Locate every Plasmodium ovale-infected red blood cell.
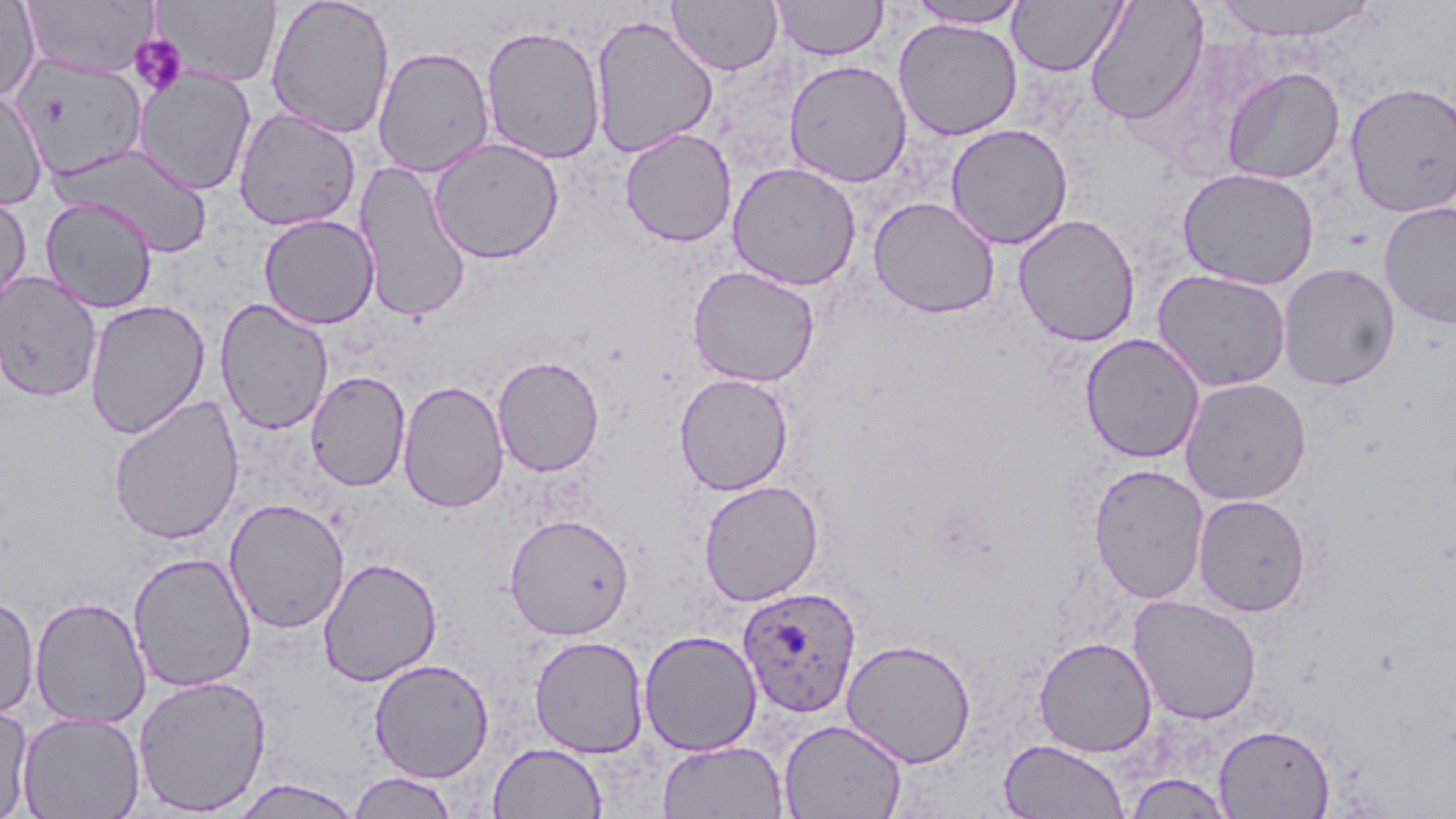
Approximate bounding boxes as named x1/y1/x2/y2 corners in pixels.
Plasmodium ovale-infected red blood cells: (x1=737, y1=587, x2=861, y2=718).

Summary:
  - Uninfected red blood cell locations: (x1=20, y1=0, x2=159, y2=79), (x1=153, y1=0, x2=284, y2=87), (x1=265, y1=0, x2=396, y2=138), (x1=772, y1=0, x2=887, y2=60), (x1=907, y1=0, x2=1030, y2=28), (x1=1007, y1=0, x2=1128, y2=76), (x1=1085, y1=0, x2=1209, y2=126), (x1=1211, y1=0, x2=1380, y2=41), (x1=0, y1=1, x2=41, y2=103), (x1=668, y1=1, x2=783, y2=75), (x1=589, y1=13, x2=720, y2=158), (x1=894, y1=18, x2=1023, y2=141), (x1=480, y1=24, x2=607, y2=165), (x1=372, y1=46, x2=495, y2=177), (x1=15, y1=56, x2=149, y2=173), (x1=784, y1=59, x2=913, y2=187), (x1=1222, y1=66, x2=1345, y2=184), (x1=133, y1=67, x2=257, y2=196), (x1=1345, y1=81, x2=1456, y2=217), (x1=0, y1=87, x2=49, y2=210), (x1=233, y1=107, x2=362, y2=231), (x1=945, y1=123, x2=1073, y2=250), (x1=619, y1=127, x2=737, y2=247), (x1=428, y1=137, x2=565, y2=264), (x1=54, y1=144, x2=214, y2=256), (x1=354, y1=159, x2=472, y2=324), (x1=727, y1=161, x2=862, y2=290), (x1=1178, y1=167, x2=1320, y2=290), (x1=0, y1=191, x2=32, y2=311), (x1=38, y1=196, x2=157, y2=313), (x1=868, y1=196, x2=1001, y2=319), (x1=1379, y1=202, x2=1456, y2=329), (x1=1013, y1=213, x2=1140, y2=347), (x1=258, y1=214, x2=380, y2=330), (x1=1277, y1=263, x2=1401, y2=390), (x1=687, y1=265, x2=821, y2=387), (x1=1152, y1=269, x2=1293, y2=392), (x1=0, y1=270, x2=102, y2=402), (x1=214, y1=298, x2=334, y2=435), (x1=84, y1=299, x2=211, y2=439), (x1=1079, y1=333, x2=1206, y2=463), (x1=492, y1=355, x2=605, y2=477), (x1=305, y1=370, x2=411, y2=491), (x1=674, y1=372, x2=794, y2=495), (x1=1179, y1=377, x2=1312, y2=506), (x1=398, y1=380, x2=510, y2=513), (x1=107, y1=393, x2=245, y2=545), (x1=1088, y1=463, x2=1210, y2=604), (x1=698, y1=480, x2=825, y2=606), (x1=1193, y1=494, x2=1312, y2=616), (x1=224, y1=498, x2=350, y2=634), (x1=504, y1=513, x2=635, y2=640), (x1=127, y1=552, x2=256, y2=693), (x1=318, y1=556, x2=443, y2=687), (x1=0, y1=593, x2=40, y2=718), (x1=1128, y1=594, x2=1263, y2=725), (x1=29, y1=596, x2=151, y2=729), (x1=638, y1=629, x2=762, y2=756), (x1=529, y1=635, x2=649, y2=758), (x1=1033, y1=636, x2=1158, y2=757), (x1=840, y1=638, x2=978, y2=767), (x1=368, y1=659, x2=494, y2=782), (x1=132, y1=674, x2=272, y2=816), (x1=0, y1=703, x2=33, y2=817), (x1=17, y1=710, x2=145, y2=819), (x1=778, y1=718, x2=908, y2=819), (x1=1214, y1=723, x2=1336, y2=818), (x1=999, y1=739, x2=1130, y2=819), (x1=657, y1=740, x2=789, y2=818), (x1=488, y1=742, x2=608, y2=818), (x1=348, y1=771, x2=459, y2=818), (x1=1125, y1=773, x2=1234, y2=818), (x1=228, y1=778, x2=364, y2=818)
  - Platelet locations: (x1=129, y1=34, x2=189, y2=97)
  - Slide-level diagnosis: Plasmodium ovale
  - Field of view: single
  - Stain: May-Grünwald-Giemsa
  - Modality: optical microscopy
  - Magnification: 1000x
  - Preparation: thin blood film
  - Image size: 1456×819 pixels